Locate every uninfected red blood cell.
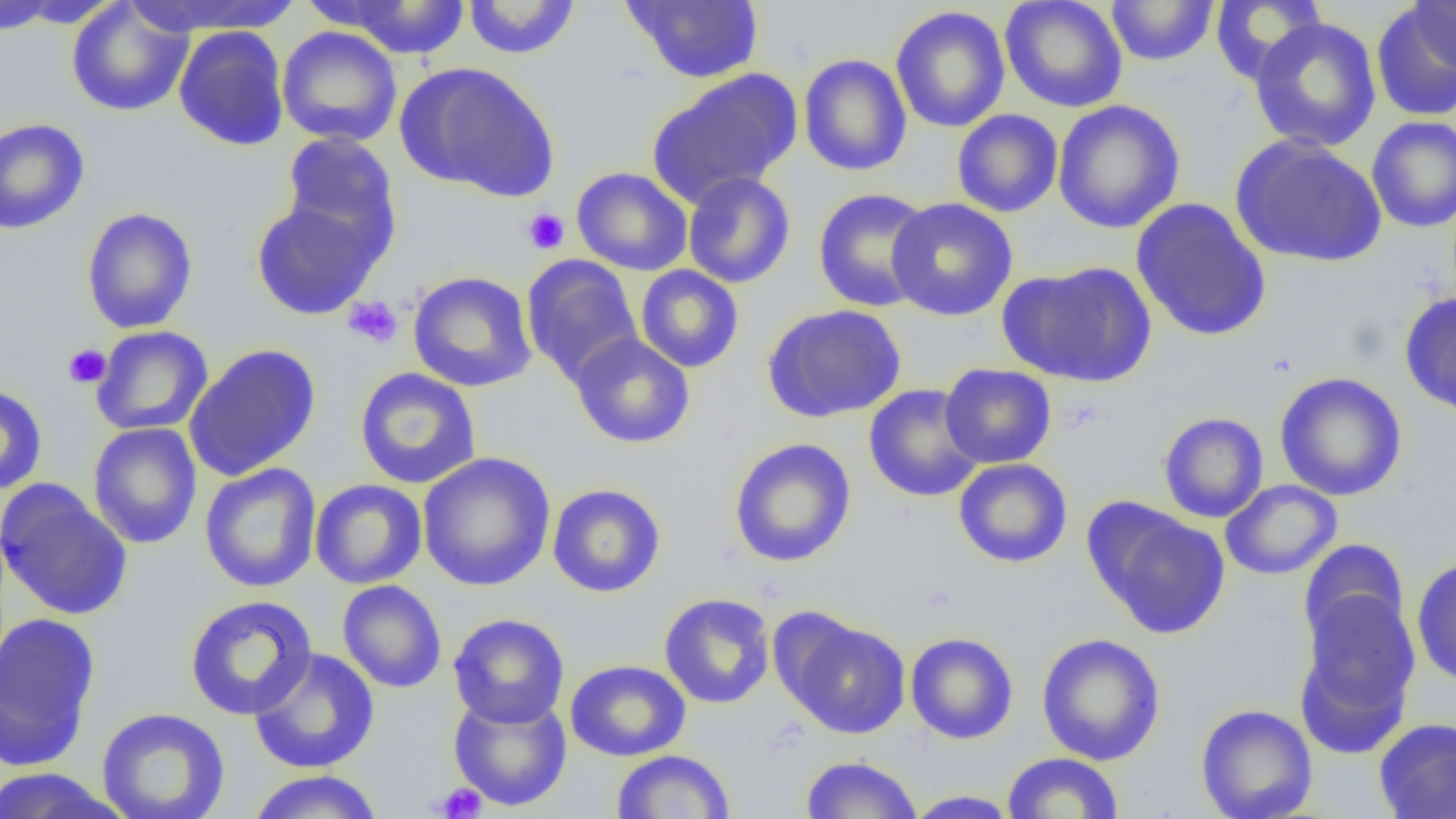

Approximate bounding boxes as [x1, y1, x2, y2] in pixels.
Uninfected red blood cells: [126, 0, 305, 36], [462, 0, 581, 59], [622, 0, 764, 84], [1000, 0, 1128, 113], [1105, 0, 1220, 66], [1409, 0, 1456, 74], [0, 1, 63, 35], [9, 1, 125, 30], [333, 1, 471, 60], [66, 2, 194, 117], [1209, 2, 1327, 84], [1370, 2, 1456, 123], [890, 6, 1010, 133], [1248, 17, 1382, 152], [173, 25, 289, 151], [276, 26, 403, 147], [798, 53, 912, 176], [398, 62, 559, 202], [647, 70, 802, 208], [1052, 99, 1185, 233], [951, 109, 1064, 217], [1366, 116, 1456, 232], [0, 118, 90, 234], [280, 131, 402, 254], [1230, 136, 1387, 268], [571, 167, 693, 275], [682, 171, 796, 289], [812, 187, 934, 313], [250, 197, 383, 320], [886, 197, 1018, 321], [1131, 197, 1272, 342], [81, 206, 198, 334], [521, 255, 643, 385], [999, 261, 1157, 387], [635, 265, 744, 373], [407, 271, 538, 392], [1400, 291, 1456, 417], [762, 304, 907, 423], [91, 326, 214, 435], [569, 332, 696, 449], [184, 343, 321, 481], [939, 363, 1056, 469], [354, 367, 482, 489], [1274, 372, 1407, 501], [864, 383, 985, 503], [0, 384, 48, 495], [1158, 412, 1269, 523], [87, 422, 203, 549], [728, 437, 856, 567], [417, 451, 556, 592], [953, 457, 1073, 568], [199, 463, 322, 593], [309, 479, 428, 589], [1220, 479, 1342, 579], [0, 480, 133, 621], [547, 484, 665, 598], [1086, 501, 1230, 639], [1297, 538, 1411, 655], [1410, 555, 1456, 688], [336, 579, 447, 693], [659, 592, 775, 709], [1295, 592, 1419, 749], [184, 595, 318, 720], [0, 612, 101, 771], [448, 613, 569, 728], [782, 616, 910, 739], [905, 632, 1019, 744], [1036, 632, 1166, 766], [248, 647, 380, 774], [565, 659, 691, 761], [448, 692, 572, 812], [1195, 703, 1318, 819], [96, 707, 230, 819], [1373, 717, 1456, 818], [611, 750, 736, 818], [1001, 752, 1124, 818], [799, 755, 923, 818], [0, 767, 129, 819], [246, 769, 383, 819], [902, 790, 1020, 818].

Summary:
  - Platelet locations: [522, 208, 570, 254], [343, 296, 403, 349], [63, 343, 111, 388], [434, 783, 488, 818]
  - Slide-level diagnosis: no evidence of blood parasites
  - Field of view: single
  - Image size: 1456×819 pixels
  - Preparation: thin blood film
  - Magnification: 1000x
  - Modality: light microscopy